Name the cell type shown.
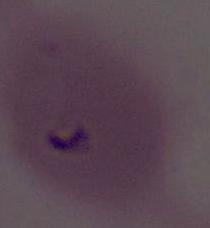

This is an erythrocyte.

modality: micrograph
magnification: 1000x